Locate every blood parasite and identify its species.
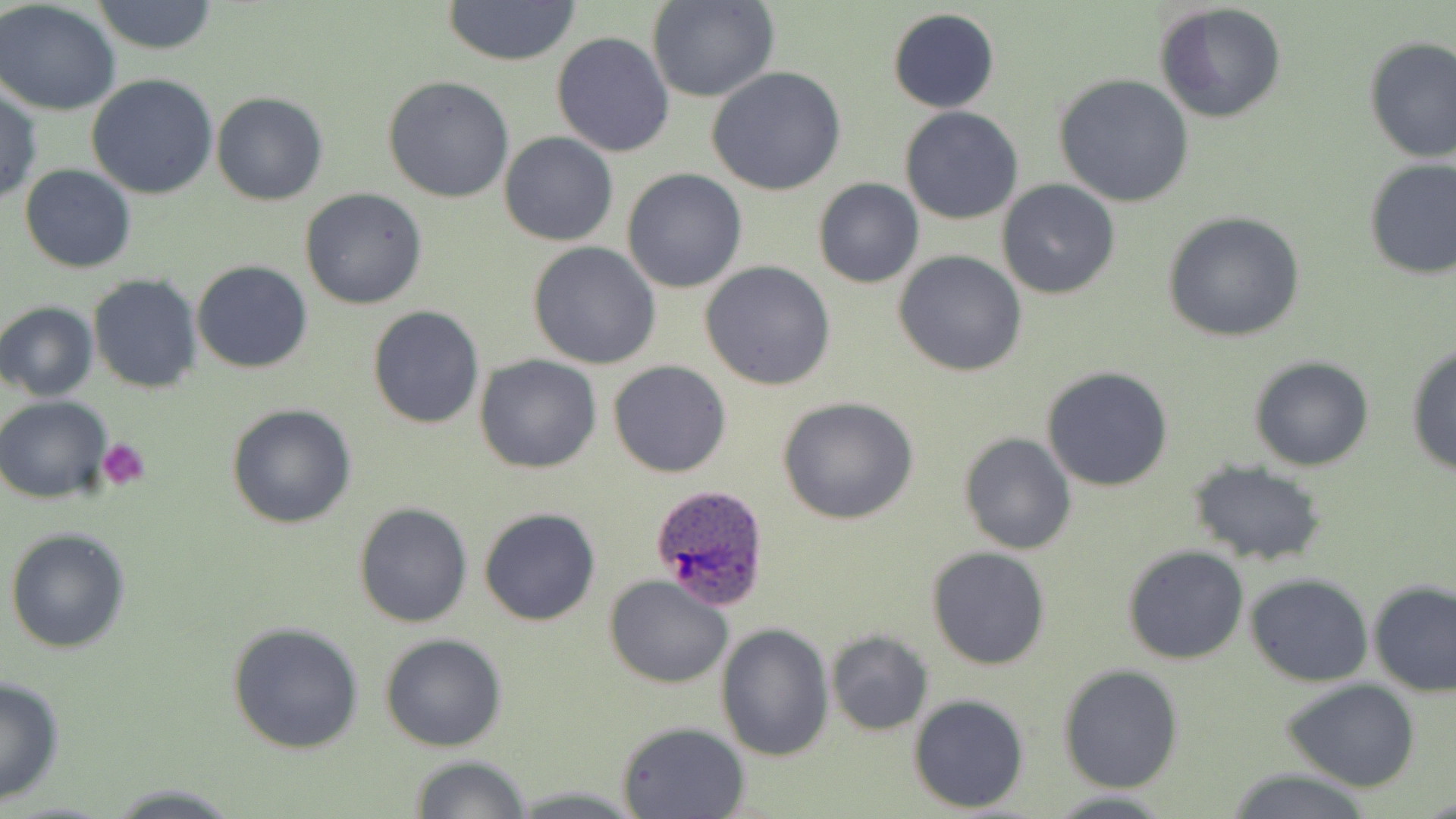
Approximate bounding boxes as (x1,y1)-(x2,y2) corner pairs in pixels.
Plasmodium ovale-infected red blood cells: (649,483)-(773,610).
No Plasmodium falciparum, Plasmodium malariae, Plasmodium vivax, Babesia divergens, or Trypanosoma brucei observed.

slide-level diagnosis = Plasmodium ovale
platelet locations = approximate bounding boxes as (x1,y1)-(x2,y2) corner pairs in pixels: (98,438)-(150,491)
magnification = 1000x
image size = 1456×819 pixels
preparation = thin blood film
stain = May-Grünwald-Giemsa
uninfected red blood cell locations = approximate bounding boxes as (x1,y1)-(x2,y2) corner pairs in pixels: (92,0)-(220,55), (650,0)-(779,102), (442,1)-(582,66), (0,2)-(120,115), (1156,2)-(1286,125), (886,8)-(1000,112), (552,32)-(675,157), (1362,36)-(1455,164), (706,67)-(848,195), (87,74)-(219,201), (1055,75)-(1194,209), (383,76)-(515,204), (0,85)-(42,205), (212,92)-(328,206), (900,106)-(1022,224), (499,131)-(618,246), (1361,156)-(1456,279), (20,163)-(137,273), (623,169)-(747,294), (813,178)-(924,288), (997,180)-(1121,301), (300,188)-(428,310), (1163,211)-(1306,343), (529,242)-(661,370), (894,250)-(1027,377), (190,260)-(312,373), (699,261)-(838,391), (87,273)-(202,394), (0,300)-(98,401), (366,305)-(485,431), (1404,345)-(1456,477), (475,355)-(602,474), (1249,355)-(1376,472), (609,360)-(731,478), (1041,366)-(1175,492), (0,395)-(113,504), (777,396)-(920,523), (225,403)-(357,530), (958,432)-(1075,555), (1186,461)-(1329,566), (353,501)-(473,629), (478,507)-(601,627), (5,526)-(131,653), (1122,545)-(1249,665), (927,547)-(1051,669), (1245,573)-(1374,686), (605,575)-(733,687), (1368,579)-(1455,697), (226,622)-(366,755), (716,622)-(834,760), (825,630)-(933,735), (381,633)-(507,751), (1058,664)-(1183,793), (0,676)-(66,804), (1281,678)-(1421,792), (908,695)-(1029,812), (616,721)-(749,818), (407,755)-(532,819), (1221,767)-(1377,819), (102,782)-(243,817), (1046,791)-(1179,819)
field of view = single
modality = light microscopy